Classify this cell by malaria status.
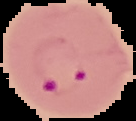
It is parasitized.

preparation = thin blood film
image type = cell region segmented out of the field of view; surrounding area masked to black
image size = 136×121 pixels